Assess this cell for malaria.
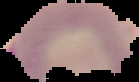
It is parasitized.

Summary:
  - Preparation: thin blood smear
  - Image type: segmented cell region on a black background
  - Image size: 139×82 pixels